Assess this cell for malaria.
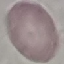

Uninfected.

{
  "stain": "Giemsa",
  "preparation": "thin blood smear",
  "image_type": "cell patch, automatically extracted from a larger field of view and resized to 64 × 64 pixels",
  "capture": "smartphone camera at the microscope eyepiece"
}